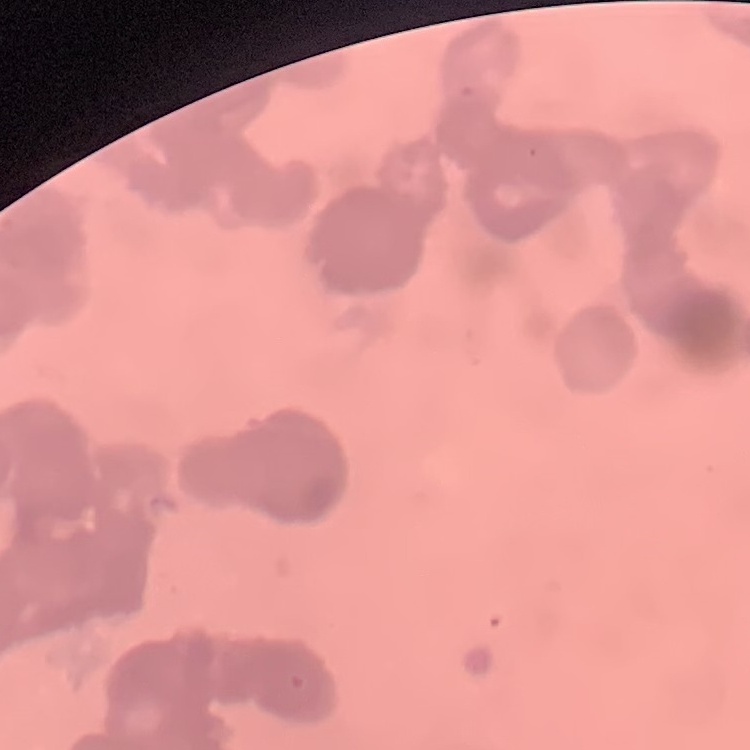

erythrocyte morphology = rouleaux formation
stain = Field's or Giemsa
preparation = thin peripheral smear
image type = square crop of a larger photomicrograph